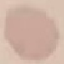 Result: no malaria parasites seen. Giemsa-stained preparation. Cell patch, automatically extracted from a larger field of view and resized to 64 × 64 pixels. Thin blood film. Photographed with a smartphone camera at the microscope eyepiece.